Identify the parasite.
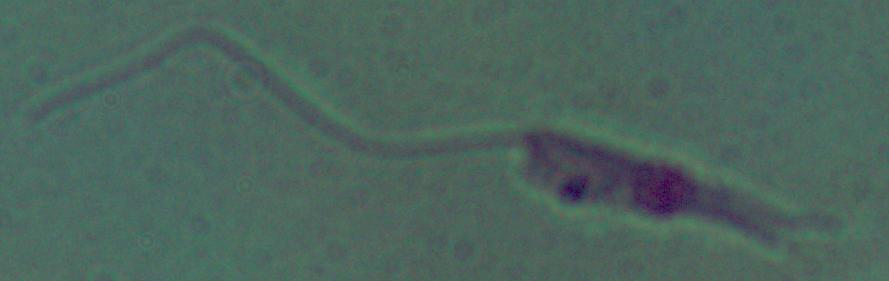

Leishmania.

Captured at 1000x magnification. Photomicrograph.